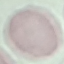
Result: no malaria parasites detected. Acquired by smartphone through the microscope eyepiece. Thin blood film. Cell patch, automatically extracted from a larger field of view and resized to 64 × 64 pixels. Giemsa-stained preparation.